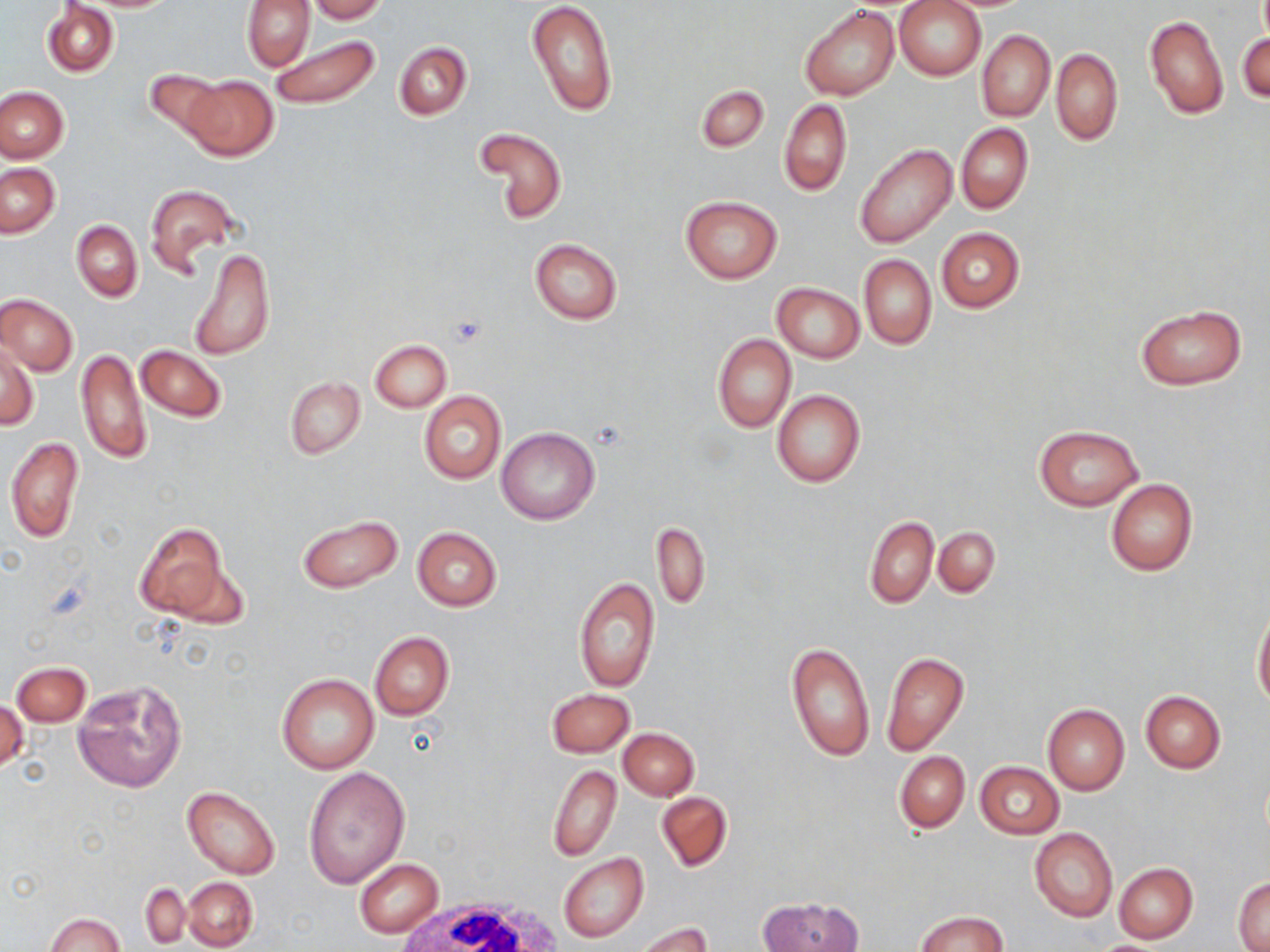

Summary:
  - Coordinate format: approximate bounding boxes as (x1,y1)-(x2,y2) corner pairs in pixels
  - White blood cell locations: (388,894)-(564,952)
  - Uninfected red blood cell locations: (307,0)-(387,22), (526,0)-(617,116), (895,0)-(985,81), (241,1)-(315,70), (43,2)-(118,77), (800,5)-(900,100), (1144,13)-(1228,118), (977,30)-(1055,121), (1238,32)-(1270,103), (269,34)-(381,111), (394,43)-(472,119), (1051,49)-(1123,145), (145,69)-(228,141), (181,75)-(278,162), (696,84)-(769,152), (0,87)-(68,162), (779,99)-(852,196), (955,122)-(1033,214), (475,127)-(568,224), (854,143)-(958,247), (1,163)-(60,237), (144,183)-(238,276), (679,195)-(782,283), (71,220)-(141,301), (936,227)-(1024,312), (529,239)-(622,324), (190,246)-(275,362), (859,254)-(936,350), (772,282)-(864,362), (1,293)-(78,376), (1135,304)-(1248,390), (712,333)-(796,432), (369,339)-(451,412), (1,343)-(38,431), (136,345)-(226,422), (76,347)-(150,466), (285,376)-(365,459), (771,390)-(866,488), (420,392)-(505,484), (1034,425)-(1142,511), (496,427)-(599,525), (5,437)-(84,544), (1105,480)-(1197,575), (296,513)-(403,594), (864,516)-(938,608), (133,522)-(231,622), (652,522)-(710,610), (934,526)-(1000,598), (411,527)-(502,611), (574,576)-(660,692), (1253,608)-(1270,710), (369,631)-(454,721), (786,642)-(874,762), (881,651)-(969,755), (13,662)-(90,726), (276,674)-(379,775), (73,679)-(187,793), (546,688)-(635,757), (1140,690)-(1225,773), (0,698)-(27,777), (1041,704)-(1129,795), (617,727)-(698,801), (894,751)-(969,832), (975,761)-(1063,839), (547,764)-(622,861), (303,767)-(409,889), (181,784)-(282,879), (656,791)-(732,872), (1029,828)-(1119,922), (559,852)-(648,943), (355,859)-(443,938), (1114,862)-(1198,943), (1233,876)-(1270,950), (181,877)-(258,951), (141,883)-(189,947), (760,897)-(863,952), (914,911)-(1010,952), (47,913)-(124,952), (635,921)-(713,952)
  - Slide-level diagnosis: negative for blood parasites
  - Magnification: 1000x
  - Image size: 1270×952 pixels
  - Preparation: thin blood smear
  - Modality: optical microscopy
  - Field of view: single
  - Stain: May-Grünwald-Giemsa